Locate and identify every blood parasite.
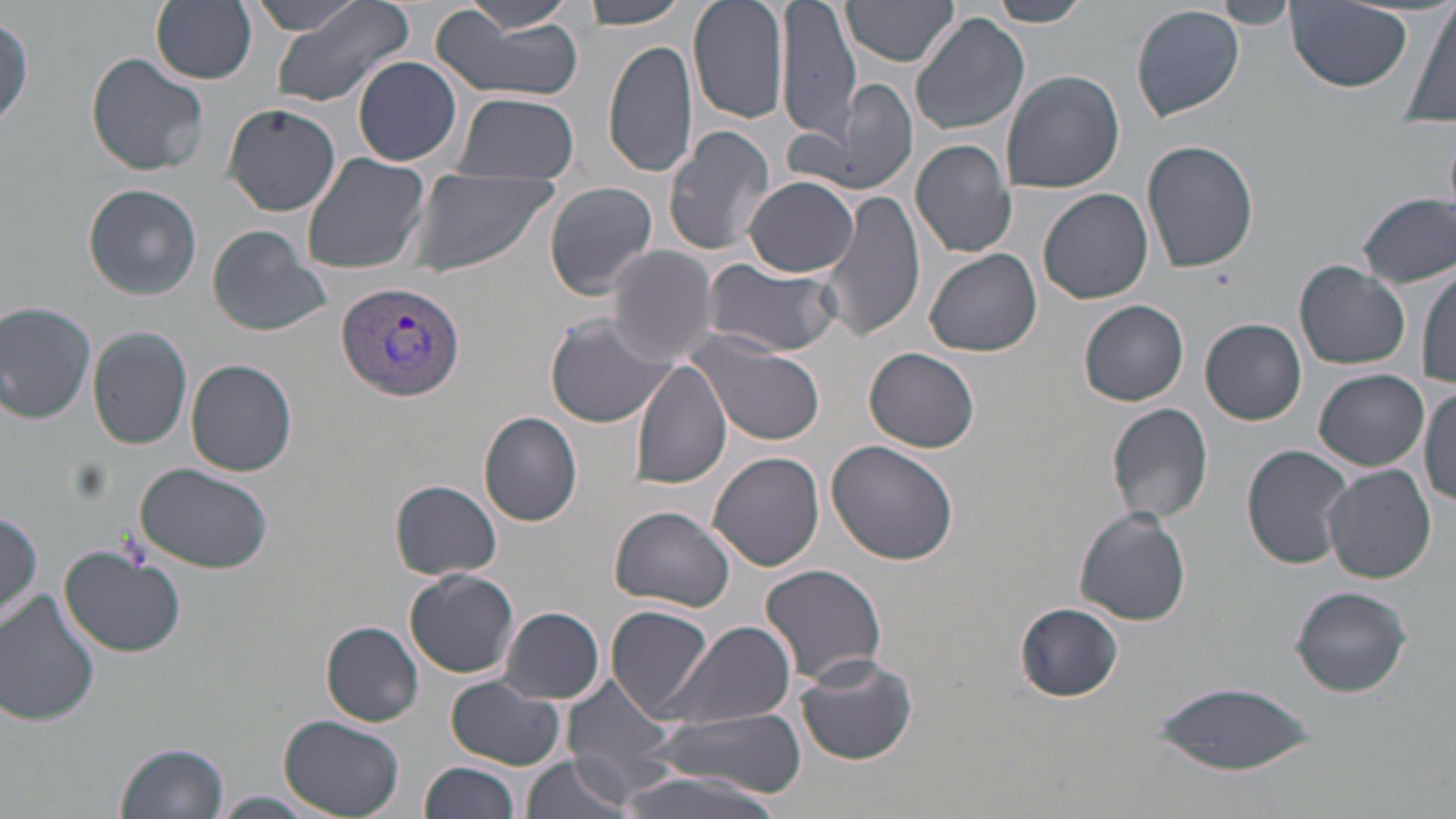
Approximate bounding boxes as [x1, y1, x2, y2] in pixels.
Plasmodium vivax-infected red blood cells: [337, 279, 466, 402].
No Plasmodium falciparum, Plasmodium ovale, Plasmodium malariae, Babesia divergens, or Trypanosoma brucei observed.

Summary:
  - Uninfected red blood cell locations: [249, 0, 372, 36], [268, 0, 416, 108], [467, 0, 573, 31], [578, 0, 691, 27], [687, 0, 790, 125], [781, 0, 859, 137], [844, 0, 959, 67], [989, 0, 1091, 26], [1214, 0, 1297, 27], [1405, 0, 1455, 126], [151, 1, 258, 84], [1287, 3, 1417, 93], [1131, 5, 1244, 122], [910, 11, 1030, 136], [432, 12, 586, 104], [0, 13, 32, 129], [602, 37, 699, 179], [85, 53, 209, 177], [352, 56, 462, 166], [1000, 69, 1124, 193], [791, 79, 920, 199], [451, 92, 579, 183], [221, 101, 341, 215], [662, 125, 776, 255], [1141, 138, 1260, 273], [909, 139, 1017, 259], [300, 152, 431, 276], [405, 169, 557, 278], [745, 176, 858, 277], [544, 182, 660, 299], [84, 183, 201, 299], [819, 186, 926, 343], [1038, 188, 1154, 304], [1357, 193, 1454, 287], [205, 224, 331, 336], [608, 246, 721, 364], [924, 249, 1043, 356], [702, 257, 845, 357], [1294, 261, 1409, 370], [1416, 264, 1455, 390], [0, 298, 99, 423], [1079, 300, 1190, 405], [544, 316, 670, 429], [1201, 319, 1306, 425], [88, 327, 192, 448], [689, 337, 824, 447], [865, 347, 981, 451], [631, 357, 733, 489], [186, 358, 298, 477], [1315, 369, 1428, 469], [1420, 386, 1456, 510], [1107, 402, 1214, 524], [480, 412, 583, 526], [827, 440, 959, 566], [1241, 445, 1355, 569], [709, 453, 825, 572], [133, 463, 275, 574], [1321, 464, 1437, 582], [390, 479, 504, 580], [609, 505, 735, 612], [1073, 507, 1191, 626], [1, 508, 45, 625], [59, 546, 188, 657], [14, 553, 136, 682], [760, 563, 888, 685], [404, 568, 520, 679], [1290, 585, 1411, 697], [1, 590, 101, 727], [1015, 602, 1124, 702], [607, 605, 716, 721], [499, 606, 606, 705], [666, 619, 796, 729], [322, 621, 425, 726], [794, 651, 918, 766], [562, 671, 679, 795], [445, 677, 565, 770], [1151, 679, 1319, 776], [645, 708, 806, 796], [278, 716, 405, 819], [116, 741, 231, 819], [520, 755, 635, 819], [422, 760, 519, 819], [607, 769, 793, 819], [212, 793, 320, 818]
  - Slide-level diagnosis: Plasmodium vivax
  - Modality: light microscopy
  - Magnification: 1000x
  - Stain: May-Grünwald-Giemsa
  - Image size: 1456×819 pixels
  - Field of view: one of a larger specimen
  - Preparation: thin blood film